Comment on the morphology of the red blood cells.
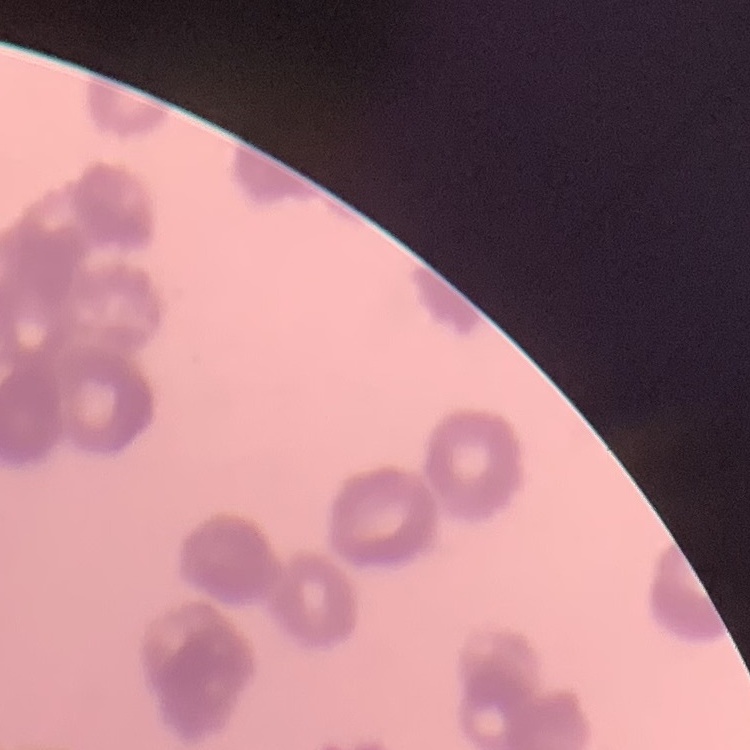

Rouleaux formation.

Summary:
  - Image type: square crop of a larger photomicrograph
  - Stain: Field's or Giemsa
  - Preparation: thin peripheral smear